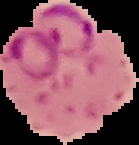

From a thin blood film. Image is 139×145 pixels. Result: malaria parasites identified. Cell region segmented out of the field of view; the surrounding area is masked to black.